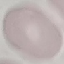 Malaria status: uninfected. Cell patch, automatically extracted from a larger field of view and resized to 64 × 64 pixels. Thin blood film. Giemsa stain. Photographed with a smartphone camera at the microscope eyepiece.